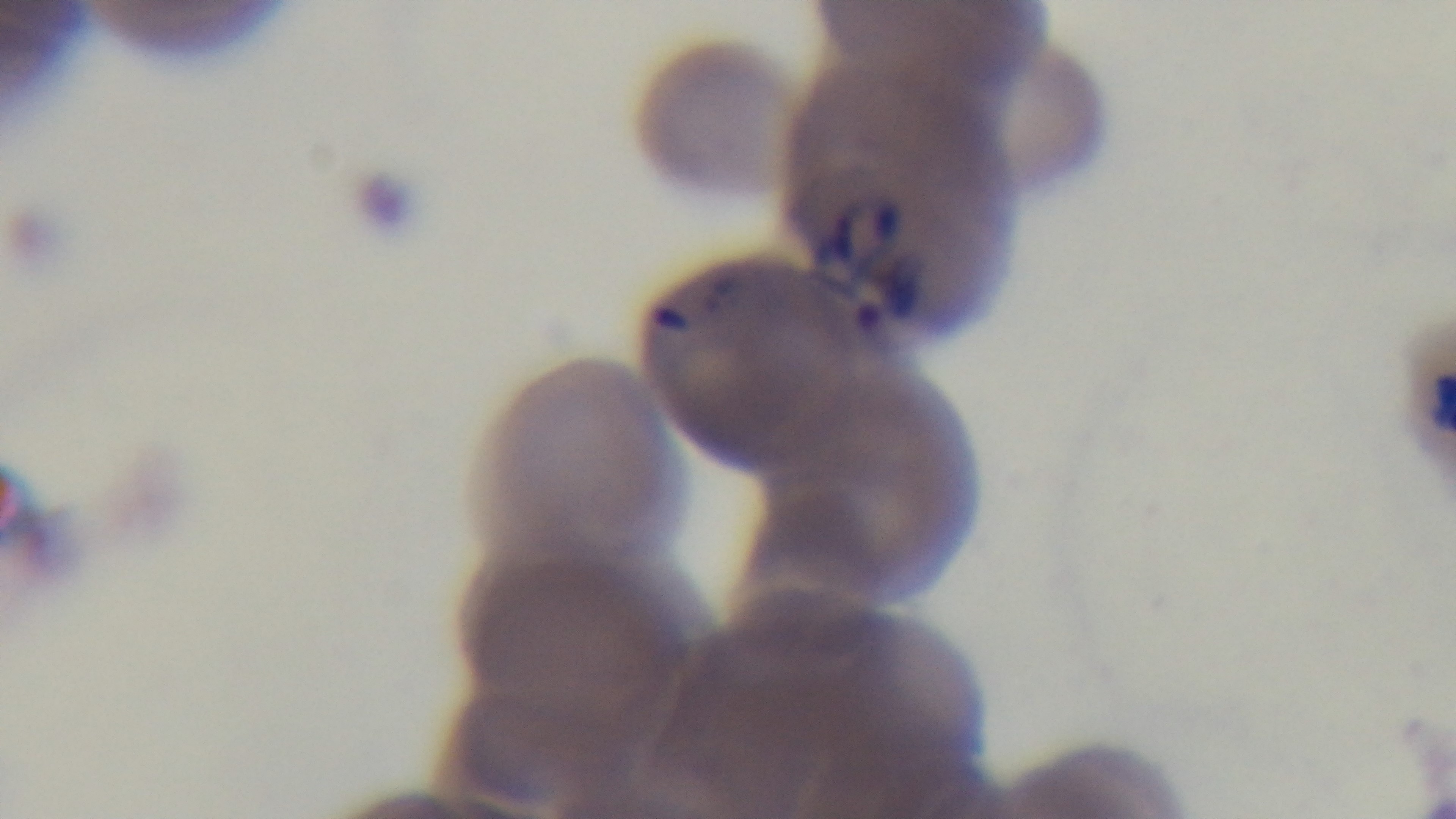
Summary:
  - Modality: light microscopy
  - Malaria status: infected
  - Field of view: one from the slide
  - Capture: mounted 4K digital camera
  - Preparation: thin smear
  - Objective: 100x oil immersion
  - Stain: Giemsa